Assess this cell for malaria.
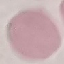

Uninfected.

capture: smartphone camera at the microscope eyepiece
image_type: automatically extracted cell patch, resized to 64 × 64 pixels
stain: Giemsa
preparation: thin smear